Name the blood parasite species.
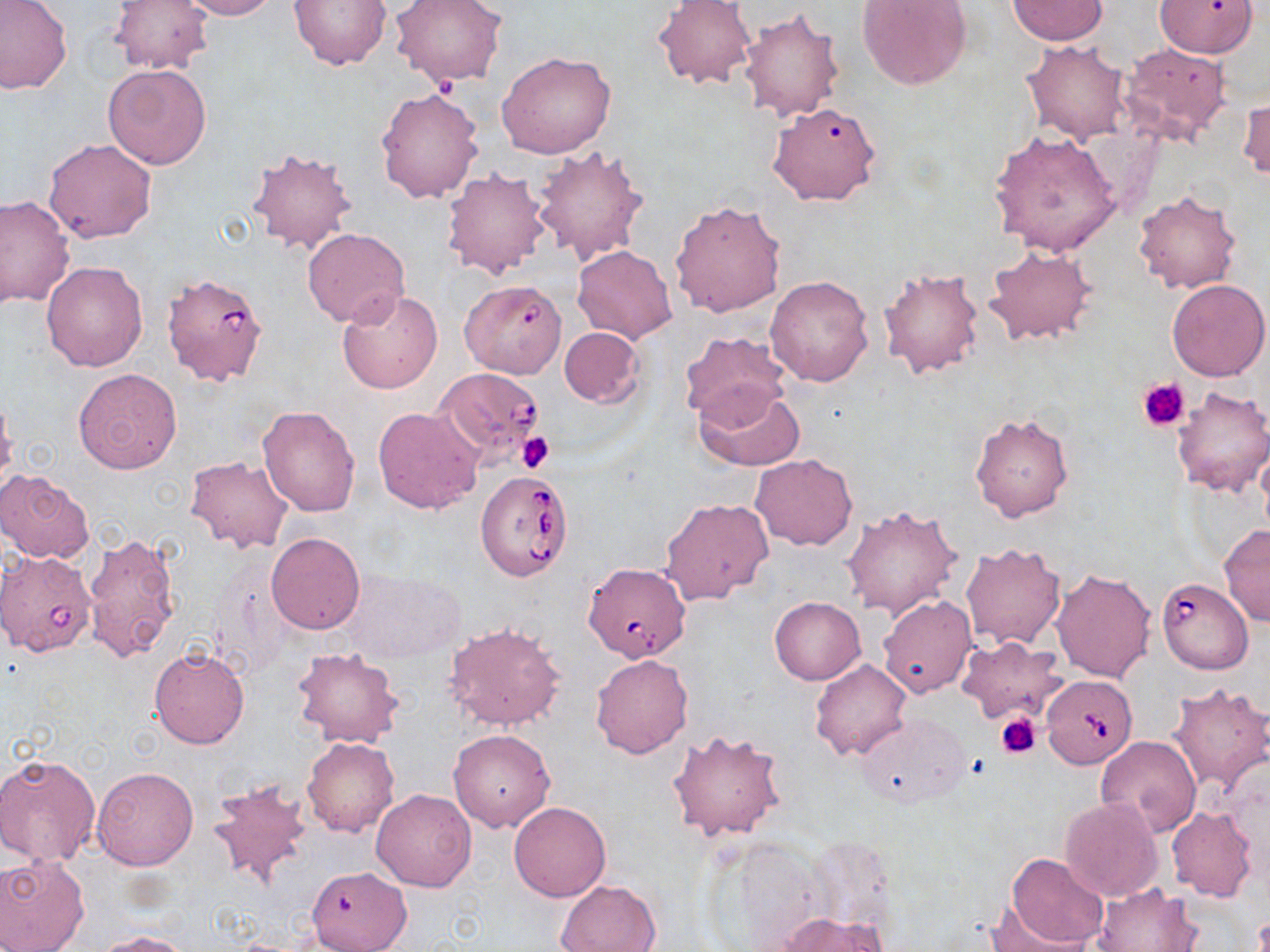

Babesia divergens.

uninfected_red_blood_cell_locations: 'approximate bounding boxes as [x1, y1, x2, y2] in pixels: [0, 0, 73, 95], [109, 0, 211, 74], [176, 0, 281, 20], [288, 0, 392, 70], [390, 0, 508, 87], [857, 0, 972, 90], [1153, 0, 1257, 57], [654, 1, 756, 90], [1008, 1, 1107, 44], [737, 9, 844, 123], [1021, 40, 1132, 144], [1118, 41, 1234, 147], [498, 50, 618, 159], [102, 63, 212, 169], [375, 86, 484, 203], [1238, 92, 1269, 184], [767, 100, 882, 206], [990, 130, 1122, 257], [43, 138, 157, 244], [532, 144, 650, 266], [246, 145, 358, 255], [442, 167, 551, 280], [1132, 188, 1242, 295], [0, 196, 74, 306], [669, 199, 786, 319], [302, 227, 410, 328], [983, 244, 1096, 345], [573, 245, 678, 344], [42, 262, 148, 370], [877, 266, 985, 380], [765, 274, 874, 385], [1166, 278, 1269, 382], [337, 288, 442, 394], [559, 327, 644, 407], [678, 331, 790, 426], [73, 368, 183, 475], [694, 382, 805, 471], [1170, 387, 1270, 497], [0, 394, 18, 493], [257, 405, 362, 517], [374, 406, 483, 514], [968, 409, 1075, 524], [1256, 442, 1270, 542], [749, 454, 856, 551], [185, 456, 295, 554], [0, 468, 95, 564], [661, 497, 774, 606], [841, 503, 962, 621], [1219, 524, 1270, 626], [80, 531, 181, 663], [265, 532, 365, 634], [959, 541, 1067, 650], [1051, 569, 1157, 683], [769, 596, 866, 684], [877, 596, 978, 698], [444, 621, 566, 732], [957, 637, 1067, 724], [149, 646, 250, 750], [292, 648, 404, 748], [590, 653, 694, 759], [810, 659, 911, 760], [1166, 681, 1269, 792], [854, 713, 972, 809], [448, 729, 556, 832], [668, 729, 789, 842], [1095, 736, 1201, 840], [303, 739, 400, 838], [0, 753, 101, 867], [91, 767, 200, 871], [207, 779, 314, 892], [370, 789, 477, 892], [1060, 797, 1162, 902], [508, 802, 611, 902], [1167, 807, 1256, 901], [1004, 852, 1110, 950], [0, 853, 90, 952], [312, 866, 413, 952], [554, 879, 663, 952], [1092, 882, 1199, 951], [984, 899, 1092, 952], [779, 913, 884, 952], [98, 932, 194, 952]'
field_of_view: one of a larger specimen
babesia_divergens_infected_red_blood_cell_locations: 'approximate bounding boxes as [x1, y1, x2, y2] in pixels: [160, 272, 271, 389], [460, 285, 568, 375], [434, 366, 546, 468], [476, 470, 574, 581], [0, 550, 97, 656], [584, 561, 691, 662], [1157, 578, 1253, 674], [1042, 674, 1138, 769]'
stain: May-Grünwald-Giemsa
preparation: thin blood film
modality: light microscopy
image_size: 1270×952 pixels
platelet_locations: 'approximate bounding boxes as [x1, y1, x2, y2] in pixels: [1138, 378, 1191, 432], [516, 433, 553, 472], [996, 712, 1042, 759]'
magnification: 1000x